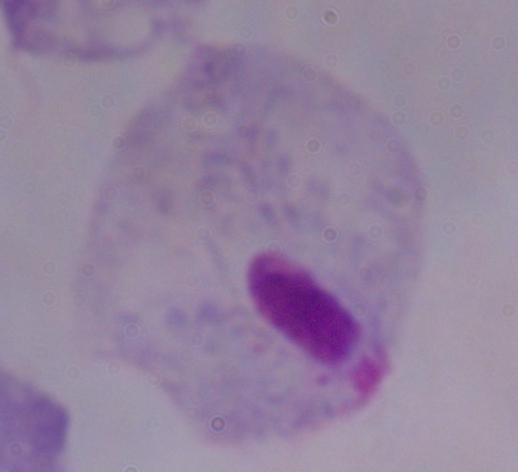
magnification = 1000x
modality = photomicrograph
identification = trichomonad